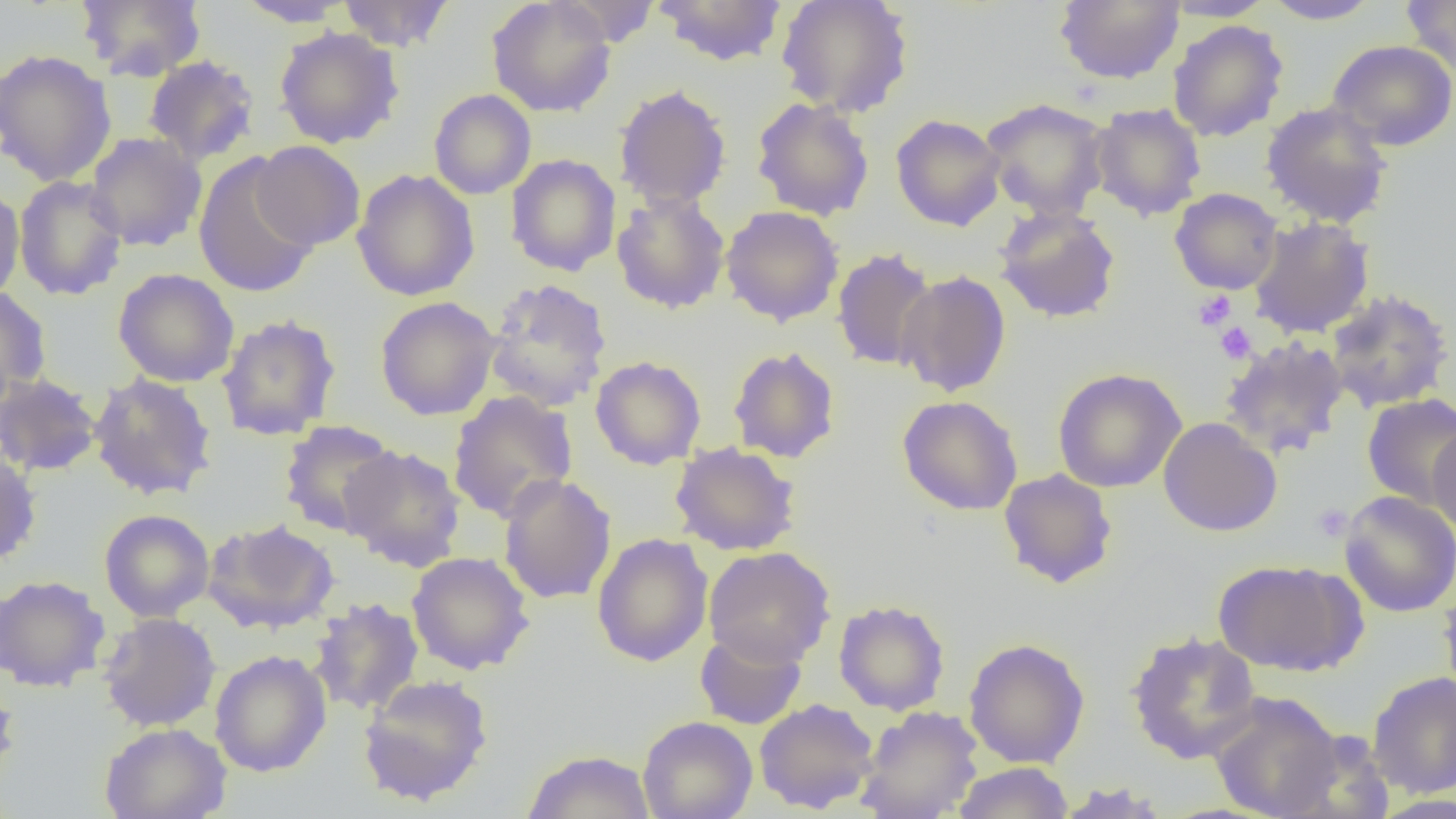
Summary:
  - Coordinate format: approximate bounding boxes as (x1,y1)-(x2,y2) corner pairs in pixels
  - Platelet locations: (1192,289)-(1236,330), (1215,321)-(1257,364), (1312,503)-(1354,541)
  - Uninfected red blood cell locations: (75,0)-(207,82), (233,0)-(356,27), (336,0)-(455,52), (486,0)-(617,118), (651,0)-(789,66), (775,0)-(914,118), (1054,0)-(1185,85), (1161,0)-(1277,21), (1260,0)-(1385,25), (1401,0)-(1456,80), (553,1)-(667,48), (1167,19)-(1289,142), (274,26)-(405,149), (1327,39)-(1456,151), (0,49)-(117,187), (142,55)-(260,167), (613,84)-(732,210), (428,89)-(537,199), (750,96)-(874,221), (980,97)-(1112,220), (1260,101)-(1394,229), (1088,102)-(1206,221), (891,113)-(1006,231), (85,133)-(207,252), (251,141)-(366,251), (192,152)-(320,300), (505,153)-(621,277), (352,168)-(480,301), (13,175)-(128,301), (0,186)-(25,304), (1170,187)-(1283,294), (612,192)-(730,314), (720,205)-(844,327), (993,205)-(1121,324), (1249,216)-(1374,338), (831,247)-(939,371), (113,268)-(240,387), (896,270)-(1012,398), (484,277)-(613,412), (0,286)-(52,406), (1324,288)-(1454,413), (375,295)-(502,421), (216,314)-(341,441), (1218,336)-(1351,458), (728,346)-(841,463), (590,356)-(706,469), (1052,367)-(1186,493), (0,373)-(102,477), (88,373)-(218,501), (447,390)-(578,523), (1361,393)-(1456,509), (896,395)-(1024,516), (1158,417)-(1283,537), (279,420)-(399,537), (1428,425)-(1456,538), (670,442)-(801,556), (339,444)-(466,571), (0,449)-(41,568), (998,468)-(1118,589), (498,473)-(617,604), (1339,490)-(1456,618), (99,508)-(214,622), (202,518)-(340,634), (592,533)-(713,667), (703,546)-(836,667), (406,551)-(534,675), (1212,558)-(1364,676), (0,574)-(110,692), (1438,579)-(1456,706), (309,597)-(424,715), (833,599)-(950,715), (98,612)-(221,732), (694,628)-(807,730), (1126,630)-(1262,764), (963,637)-(1090,768), (210,650)-(331,777), (1367,671)-(1456,798), (0,673)-(20,793), (358,674)-(494,807), (1208,691)-(1344,818), (754,698)-(879,813), (856,705)-(983,819), (638,715)-(758,819), (99,722)-(232,819), (1278,731)-(1397,819), (521,750)-(656,819), (951,762)-(1074,819), (1051,782)-(1173,818)
  - Slide-level diagnosis: no evidence of blood parasites
  - Magnification: 1000x
  - Field of view: single
  - Preparation: thin blood smear
  - Modality: light microscopy
  - Image size: 1456×819 pixels